State the blood parasite species.
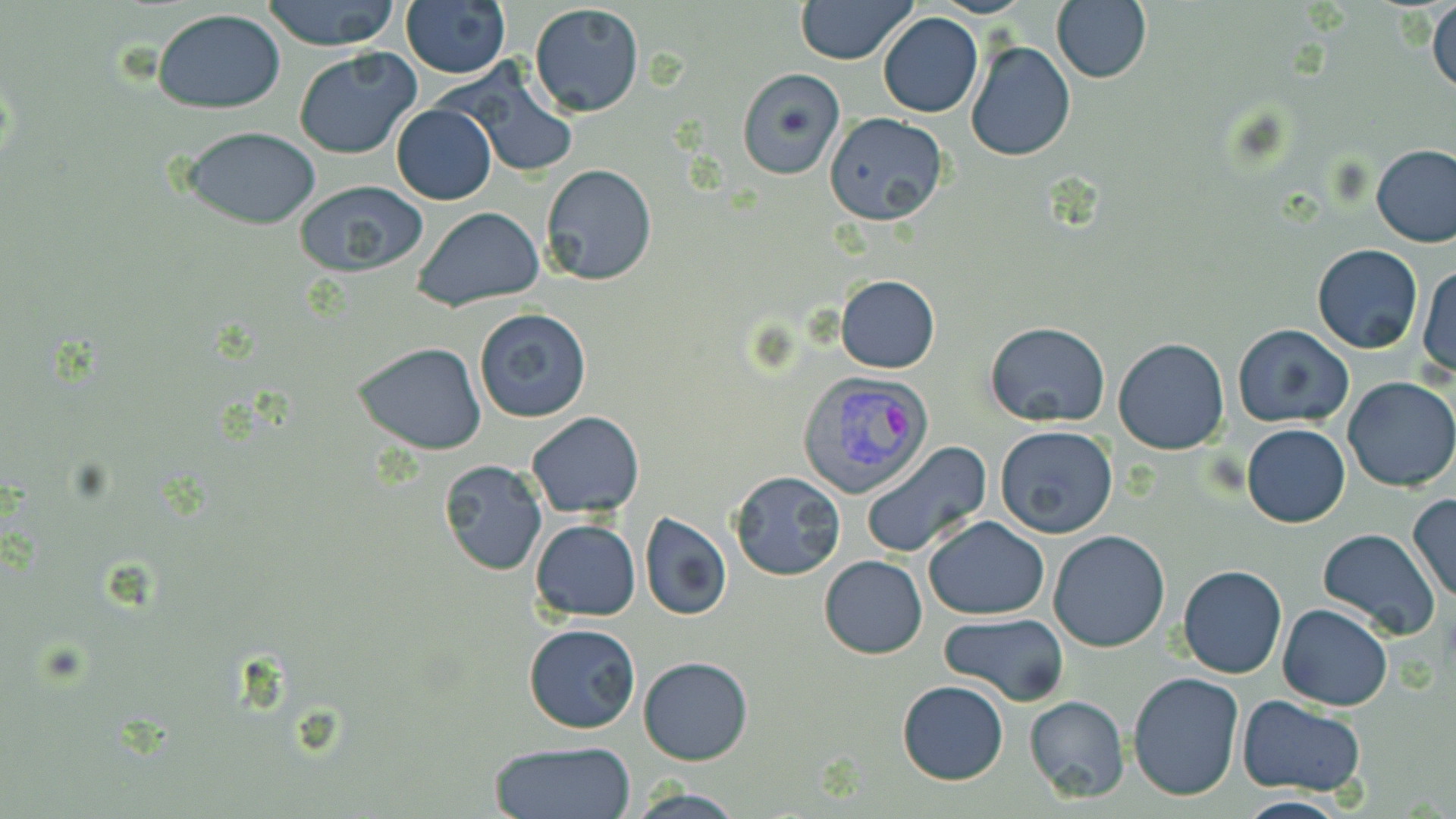

Plasmodium vivax.

Approximate bounding boxes as (x1, y1, x2, y2) in pixels. Uninfected red blood cell locations: (261, 0, 404, 50), (796, 0, 916, 64), (1051, 0, 1153, 84), (1428, 0, 1456, 97), (401, 2, 512, 78), (528, 3, 646, 118), (152, 7, 286, 114), (878, 12, 983, 118), (965, 40, 1076, 162), (294, 48, 423, 160), (443, 60, 579, 180), (736, 68, 844, 179), (390, 103, 496, 205), (824, 111, 950, 225), (181, 126, 322, 228), (1372, 143, 1456, 248), (539, 165, 658, 285), (291, 181, 428, 279), (412, 207, 544, 309), (1312, 245, 1424, 353), (1416, 263, 1455, 383), (837, 274, 940, 373), (473, 307, 593, 424), (985, 322, 1110, 427), (1232, 324, 1355, 430), (1113, 338, 1229, 454), (352, 343, 488, 456), (1343, 376, 1456, 491), (526, 411, 644, 519), (1242, 424, 1351, 529), (994, 425, 1118, 537), (862, 441, 992, 558), (438, 460, 547, 575), (729, 471, 846, 581), (1407, 493, 1456, 601), (639, 511, 732, 621), (922, 515, 1050, 620), (531, 518, 641, 622), (1318, 528, 1440, 643), (1048, 530, 1170, 652), (819, 554, 928, 658), (1177, 564, 1287, 678), (1277, 602, 1393, 713), (938, 612, 1070, 707), (522, 624, 641, 733), (638, 656, 754, 766), (1126, 671, 1244, 801), (896, 680, 1009, 785), (1024, 695, 1130, 802), (1235, 696, 1368, 796), (488, 739, 637, 819), (625, 788, 747, 819), (1232, 795, 1352, 819). Plasmodium vivax-infected red blood cell locations: (797, 370, 933, 503). Captured at 1000x magnification. Thin blood smear. Light microscopy. Image is 1456×819 pixels. May-Grünwald-Giemsa-stained preparation. One field of a larger specimen.